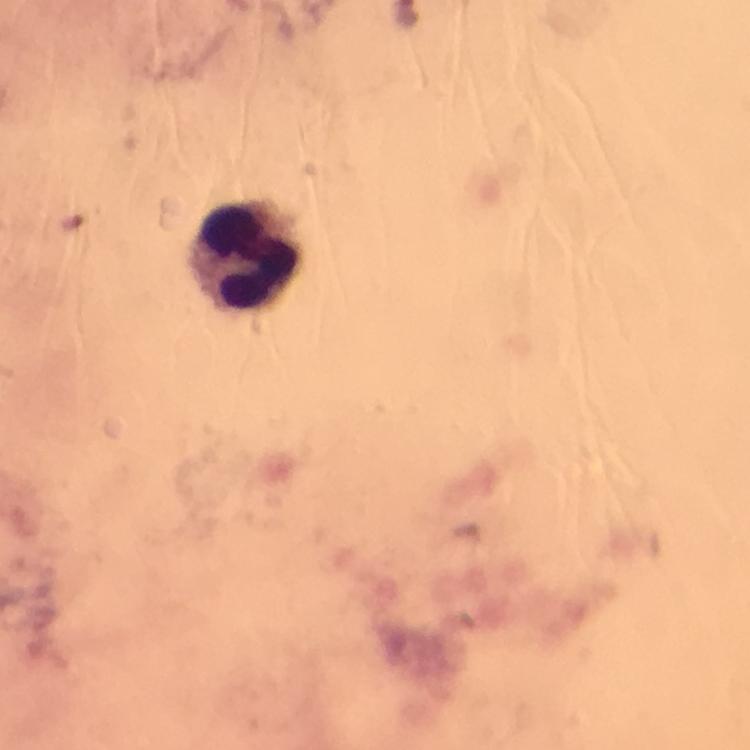
preparation: thick smear
magnification: 100x
stain: Giemsa
cropped_from: one field of view
leukocyte_locations: 'approximate centers as (x, y) in pixels: (247, 258)'
image_size: 750×750 pixels
malaria_parasites: none seen
capture: smartphone photograph through a microscope
context: from a diagnostic examination for malaria
immersion_oil: used